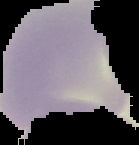
result = no malaria parasites seen
image type = segmented cell region on a black background
preparation = thin blood film
image size = 139×145 pixels